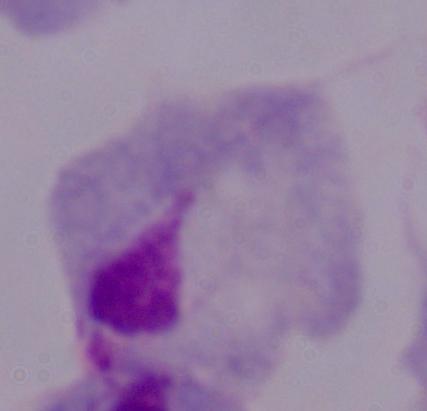

Photomicrograph. 1000x magnification. A trichomonad is shown.